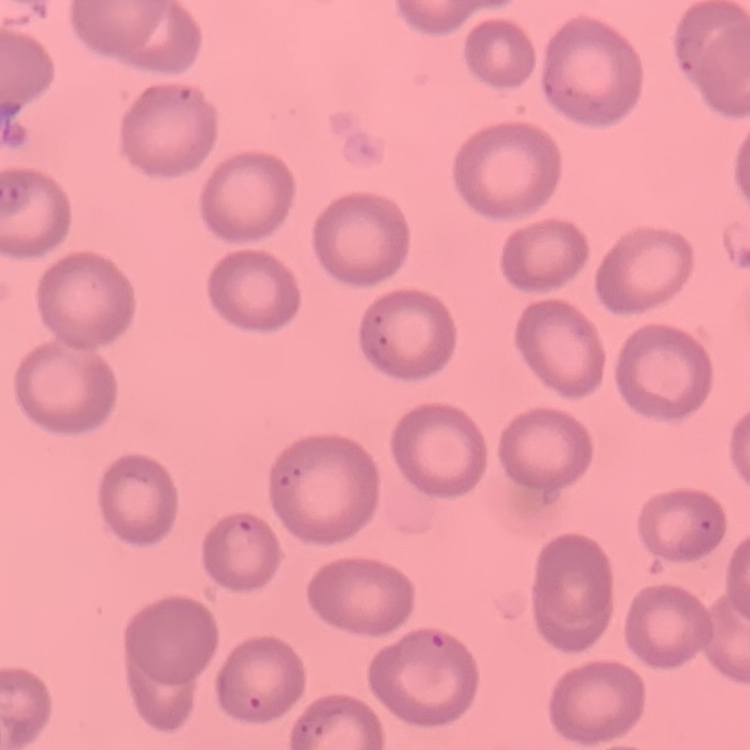
The erythrocytes exhibit no rouleaux formation. Thin blood smear. Field's or Giemsa stain. Square crop of a larger photomicrograph.